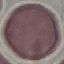

Result: no malaria parasites detected. Thin smear of blood. Automatically extracted cell patch, resized to 64 × 64 pixels. Giemsa stain. Photographed with a smartphone camera at the microscope eyepiece.